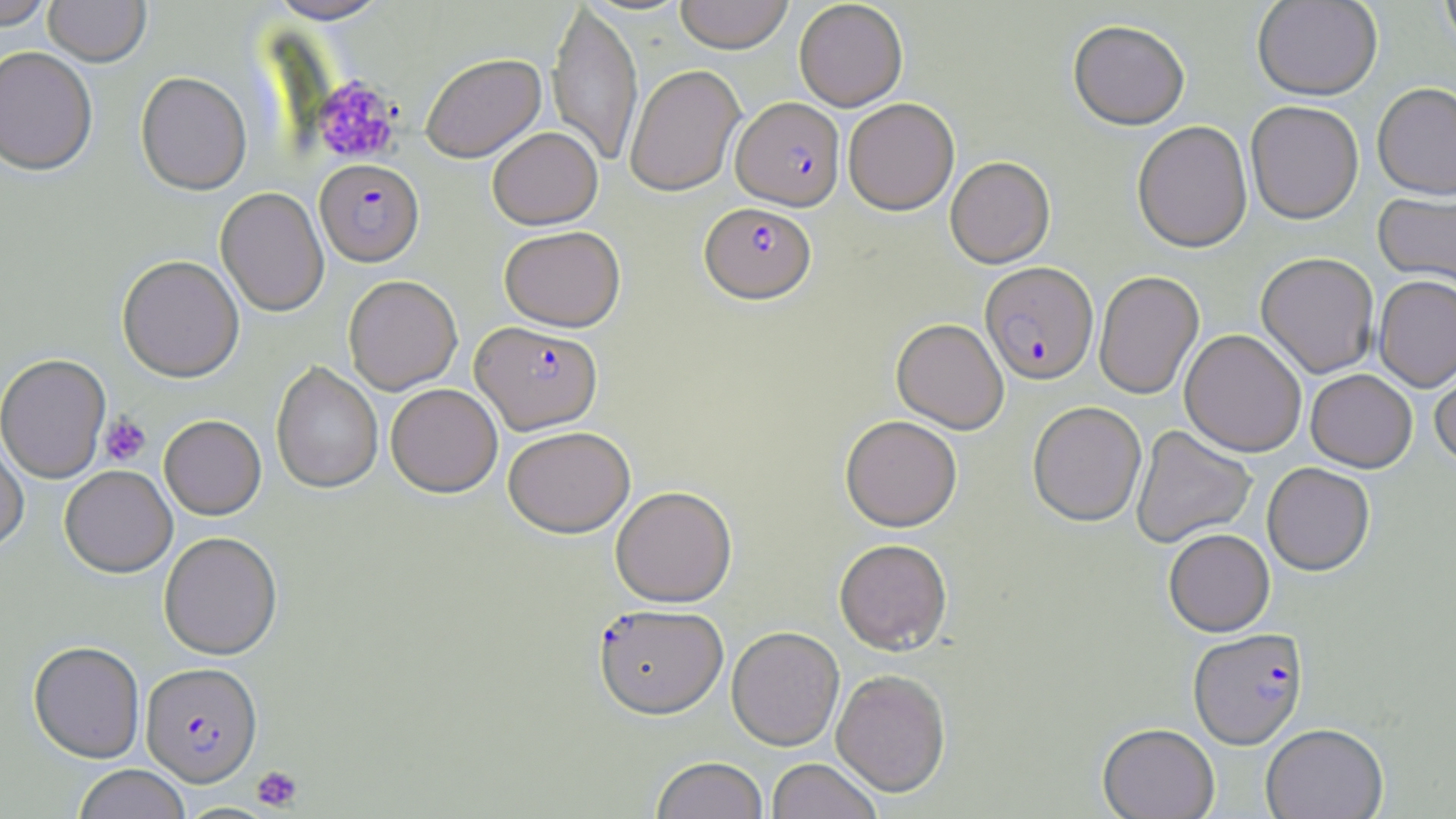

Plasmodium falciparum-infected red blood cell locations = approximate bounding boxes as [x1, y1, x2, y2] in pixels: [732, 96, 844, 210], [315, 158, 424, 266], [700, 201, 816, 303], [981, 261, 1098, 384], [472, 321, 602, 434], [595, 605, 729, 720], [1188, 628, 1308, 749], [140, 662, 262, 786]
slide-level diagnosis = Plasmodium falciparum
image size = 1456×819 pixels
uninfected red blood cell locations = approximate bounding boxes as [x1, y1, x2, y2] in pixels: [1, 0, 55, 29], [44, 0, 151, 66], [265, 0, 392, 23], [547, 0, 643, 169], [674, 0, 794, 54], [1252, 0, 1382, 101], [1439, 0, 1456, 58], [794, 1, 907, 111], [1068, 20, 1190, 131], [0, 46, 98, 175], [421, 52, 546, 162], [625, 64, 745, 197], [135, 72, 251, 195], [1372, 83, 1456, 200], [843, 98, 959, 215], [1245, 100, 1364, 224], [1132, 120, 1253, 253], [487, 127, 603, 229], [945, 156, 1055, 268], [216, 187, 329, 317], [1373, 190, 1456, 292], [499, 225, 625, 331], [1256, 252, 1379, 378], [117, 255, 244, 382], [1094, 271, 1204, 400], [343, 275, 462, 395], [1374, 275, 1456, 392], [891, 318, 1009, 433], [1180, 329, 1307, 457], [0, 353, 111, 483], [1430, 357, 1456, 468], [271, 361, 383, 494], [1305, 369, 1417, 472], [386, 383, 502, 497], [1027, 401, 1146, 526], [160, 415, 266, 519], [840, 415, 963, 531], [1130, 425, 1256, 548], [503, 426, 635, 538], [0, 430, 29, 554], [1262, 462, 1375, 576], [60, 465, 177, 577], [610, 485, 737, 607], [1163, 528, 1275, 636], [159, 531, 283, 660], [834, 538, 952, 655], [727, 626, 845, 751], [28, 641, 145, 763], [831, 669, 951, 798], [1097, 723, 1220, 819], [1260, 723, 1388, 819], [651, 757, 768, 819], [767, 759, 881, 819], [72, 765, 191, 819]
preparation = thin blood film
modality = light microscopy
stain = May-Grünwald-Giemsa
magnification = 1000x
field of view = single
platelet locations = approximate bounding boxes as [x1, y1, x2, y2] in pixels: [312, 76, 401, 165], [100, 413, 151, 466], [251, 765, 303, 811]